Give the extent of all Plasmodium ovale-infected red blood cells.
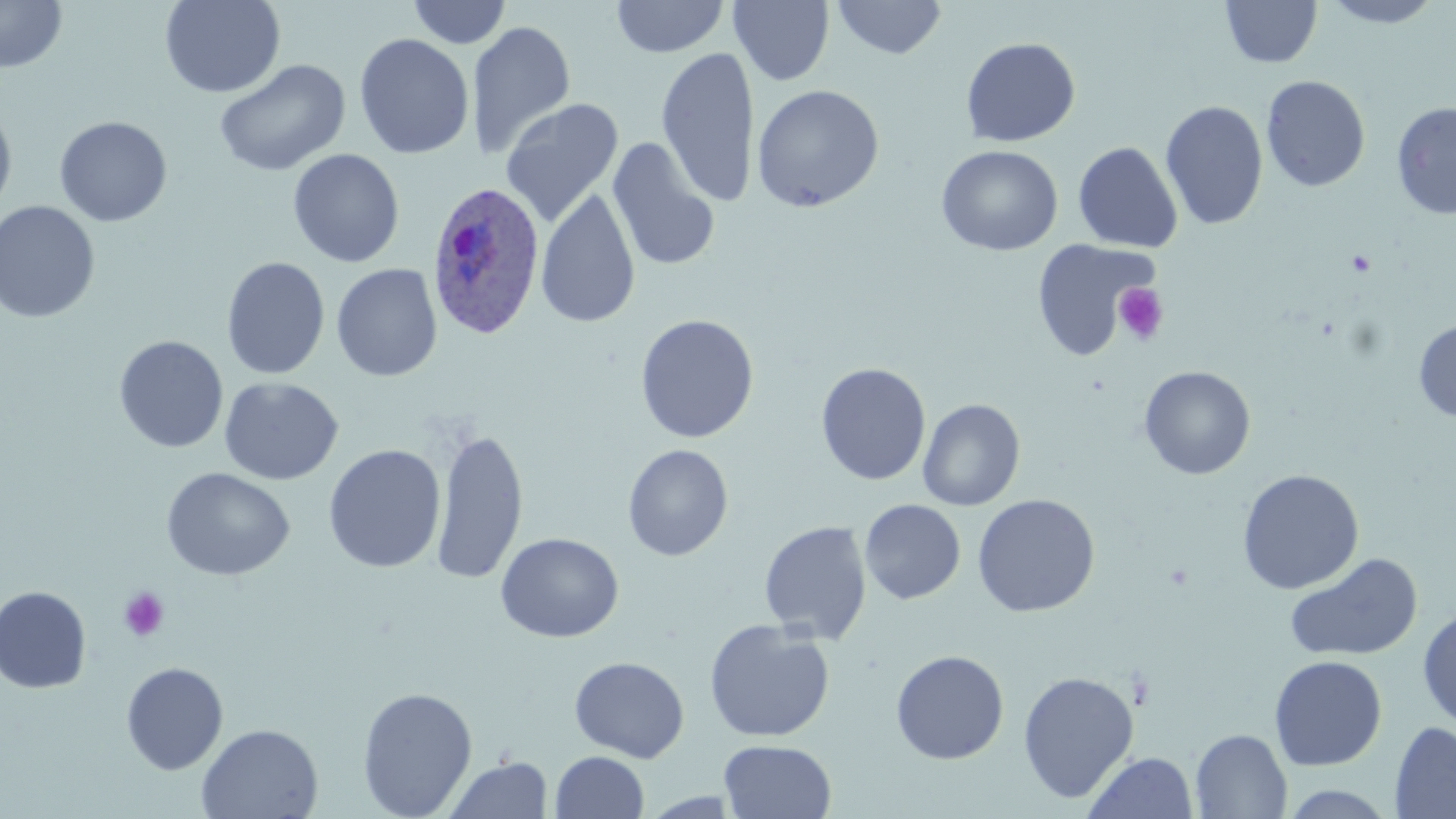

Approximate bounding boxes as (x1, y1, x2, y2) in pixels.
Plasmodium ovale-infected red blood cells: (426, 179, 547, 340).

Summary:
  - Uninfected red blood cell locations: (159, 0, 285, 98), (407, 0, 512, 49), (611, 0, 729, 58), (729, 0, 834, 86), (831, 0, 947, 60), (1220, 0, 1322, 68), (1317, 0, 1447, 28), (0, 1, 67, 74), (730, 1, 946, 76), (467, 20, 576, 158), (354, 33, 475, 160), (960, 37, 1081, 147), (657, 46, 761, 207), (214, 59, 350, 177), (1261, 75, 1371, 192), (751, 84, 885, 213), (500, 97, 623, 229), (0, 99, 17, 218), (1160, 100, 1269, 231), (1391, 101, 1456, 220), (54, 116, 173, 227), (607, 138, 720, 273), (1073, 142, 1183, 253), (936, 145, 1063, 256), (287, 148, 404, 268), (535, 187, 641, 329), (0, 201, 101, 323), (1031, 240, 1156, 360), (221, 256, 330, 380), (331, 264, 442, 382), (635, 314, 759, 443), (1413, 319, 1456, 423), (114, 335, 228, 453), (815, 362, 931, 486), (1138, 366, 1255, 480), (219, 376, 343, 486), (917, 398, 1025, 510), (432, 426, 529, 586), (323, 444, 446, 573), (623, 444, 733, 561), (162, 467, 295, 581), (1237, 469, 1364, 594), (972, 494, 1100, 617), (860, 499, 965, 604), (759, 521, 872, 643), (496, 532, 624, 643), (1284, 552, 1423, 663), (0, 585, 92, 694), (1417, 609, 1456, 732), (704, 619, 835, 742), (890, 649, 1010, 764), (1269, 655, 1387, 771), (569, 656, 690, 762), (120, 662, 229, 775), (1018, 670, 1139, 803), (357, 686, 477, 818), (1390, 721, 1456, 818), (196, 723, 323, 818), (1190, 729, 1292, 818), (719, 739, 836, 819), (550, 751, 649, 819), (1083, 751, 1199, 819), (443, 757, 552, 818), (1277, 784, 1402, 818)
  - Platelet locations: (1113, 283, 1169, 344), (118, 587, 169, 642)
  - Slide-level diagnosis: Plasmodium ovale
  - Stain: May-Grünwald-Giemsa
  - Magnification: 1000x
  - Image size: 1456×819 pixels
  - Preparation: thin blood smear
  - Modality: light microscopy
  - Field of view: single